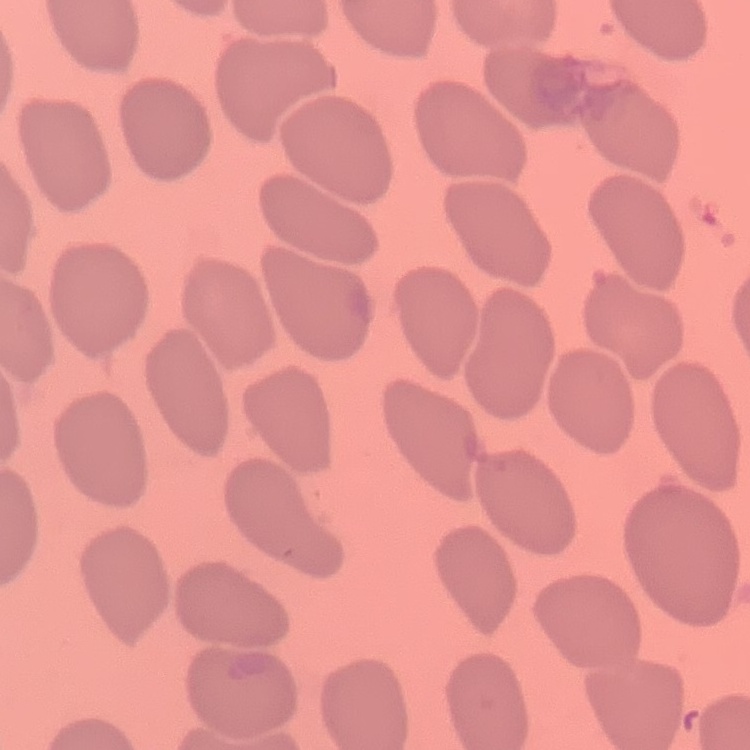
The red blood cells exhibit no rouleaux formation. Thin blood smear. Square crop of a larger photomicrograph. Stained with either Field's or Giemsa.